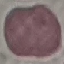
{
  "malaria_status": "uninfected",
  "stain": "Giemsa",
  "image_type": "cell patch, automatically extracted from a larger field of view and resized to 64 × 64 pixels",
  "preparation": "thin blood film",
  "capture": "smartphone through the microscope eyepiece"
}